Describe the morphology of the erythrocytes.
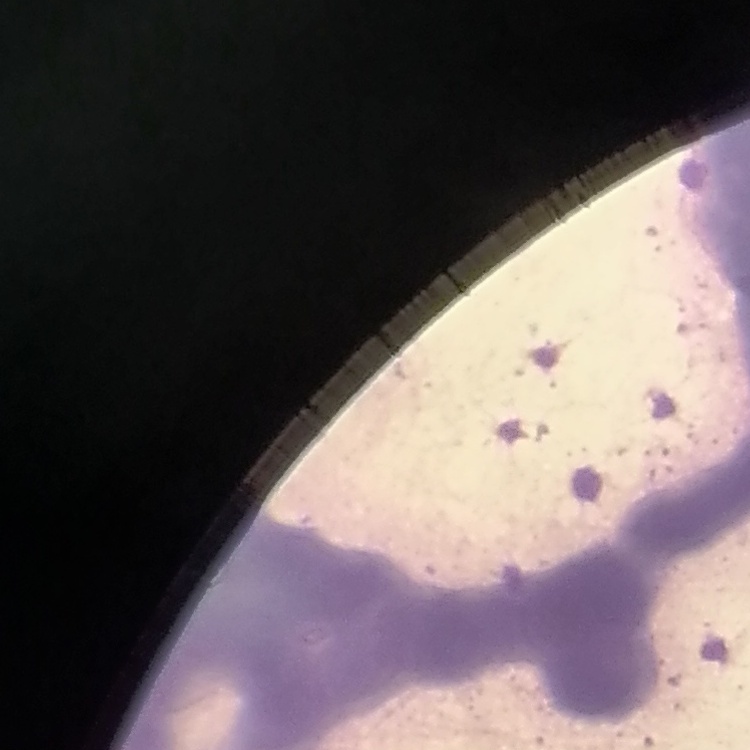

They show rouleaux formation.

Square crop of a larger photomicrograph. Stained with either Field's or Giemsa. Thin blood smear.